Classify this cell by malaria status.
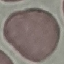

It is uninfected.

Summary:
  - Image type: cell patch, automatically extracted from a larger field of view and resized to 64 × 64 pixels
  - Capture: smartphone through the microscope eyepiece
  - Stain: Giemsa
  - Preparation: thin blood smear